Describe the morphology of the erythrocytes.
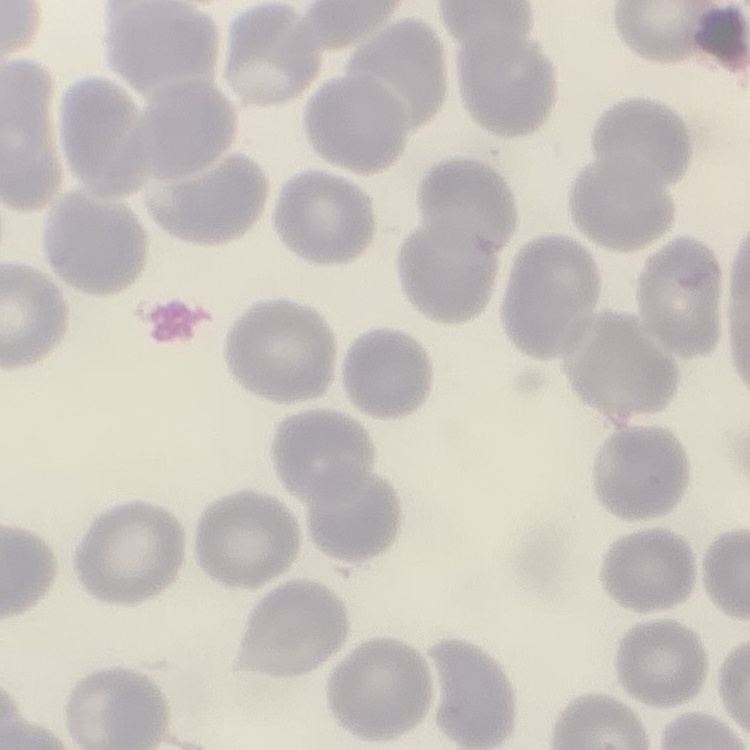
No rouleaux formation.

Thin blood film. Field's or Giemsa stain. Square crop of a larger photomicrograph.